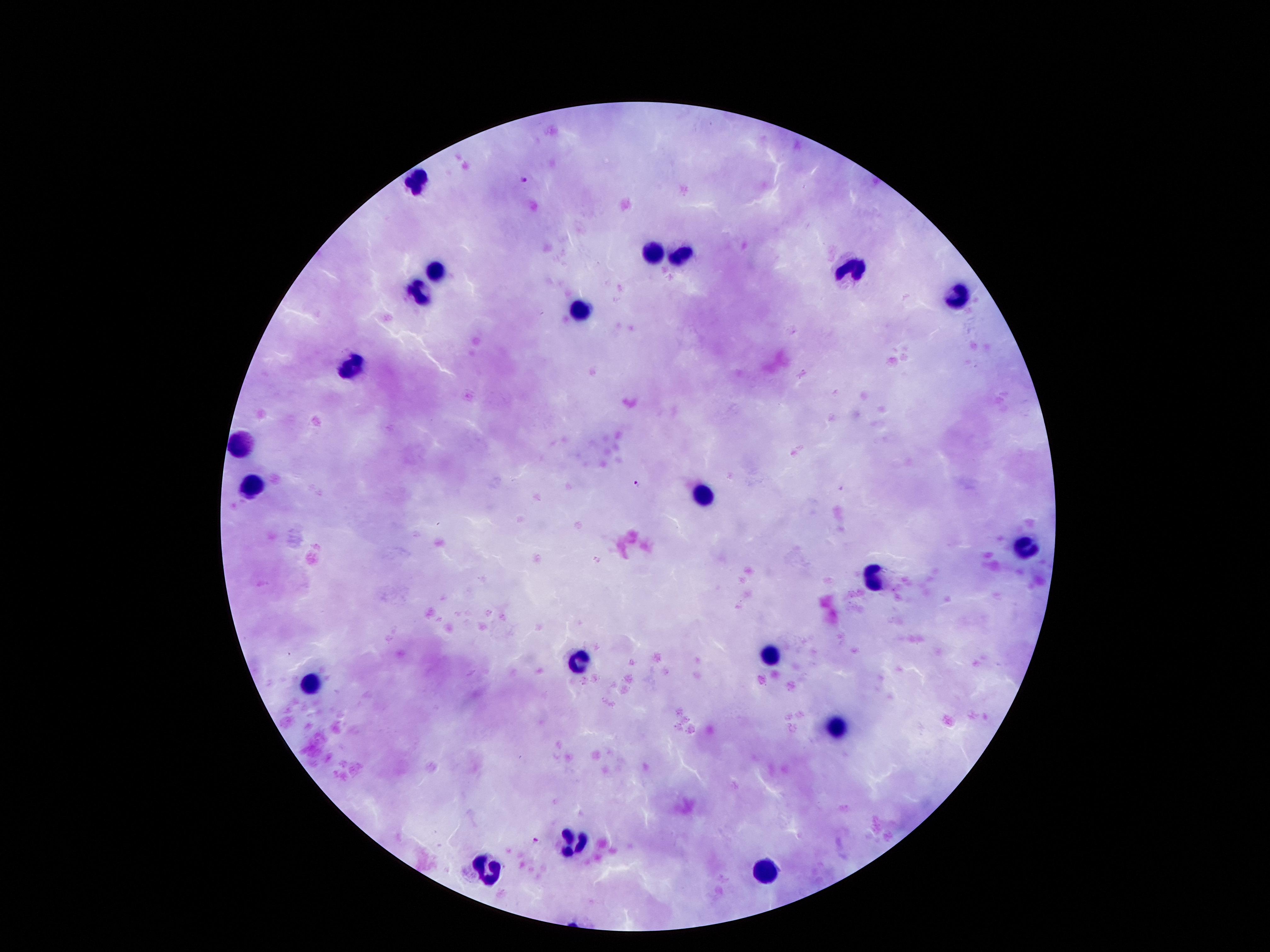

Approximate object centers, in pixels from the top-left corner. Plasmodium parasite locations: (x=523, y=179), (x=637, y=482), (x=537, y=838). Leukocyte locations: (x=416, y=178), (x=650, y=251), (x=682, y=255), (x=853, y=268), (x=436, y=271), (x=421, y=295), (x=956, y=303), (x=582, y=309), (x=352, y=369), (x=244, y=443), (x=250, y=487), (x=703, y=495), (x=1022, y=546), (x=871, y=580), (x=772, y=651), (x=582, y=660), (x=307, y=687), (x=837, y=725), (x=573, y=840), (x=488, y=869), (x=765, y=874). Smartphone photograph taken through the microscope eyepiece. Thick blood smear. Single field of view. Giemsa-stained preparation. Patient malaria status: infected with Plasmodium falciparum. 100x magnification. Image is 1270×952 pixels.